Identify the preparation type.
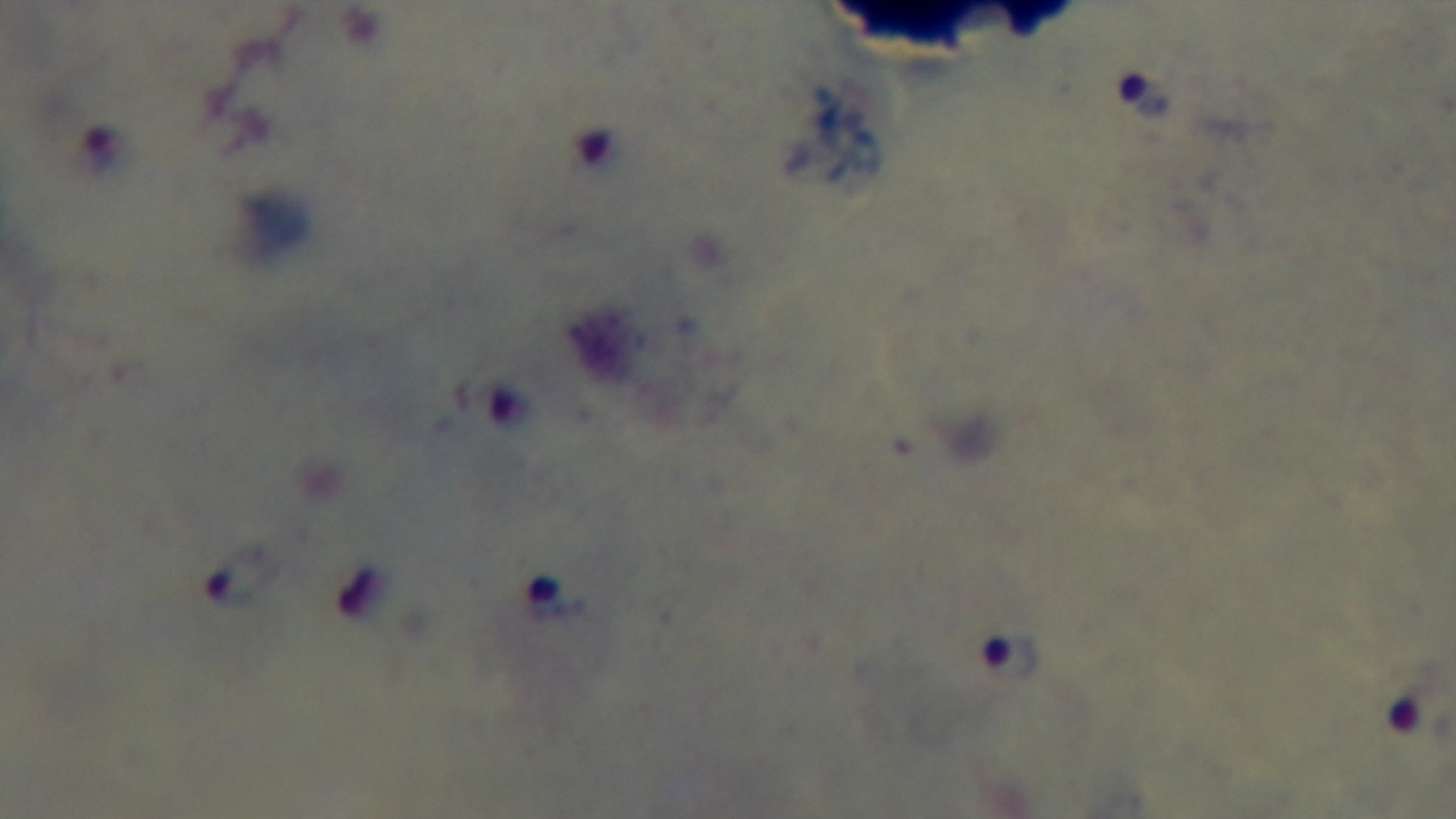
Thick.

field of view = single
modality = light microscopy
capture = mounted 4K digital camera
stain = Giemsa
objective = 100x oil immersion
malaria status = positive